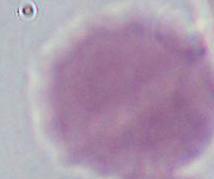

Micrograph. An erythrocyte is seen. Captured at 1000x magnification.